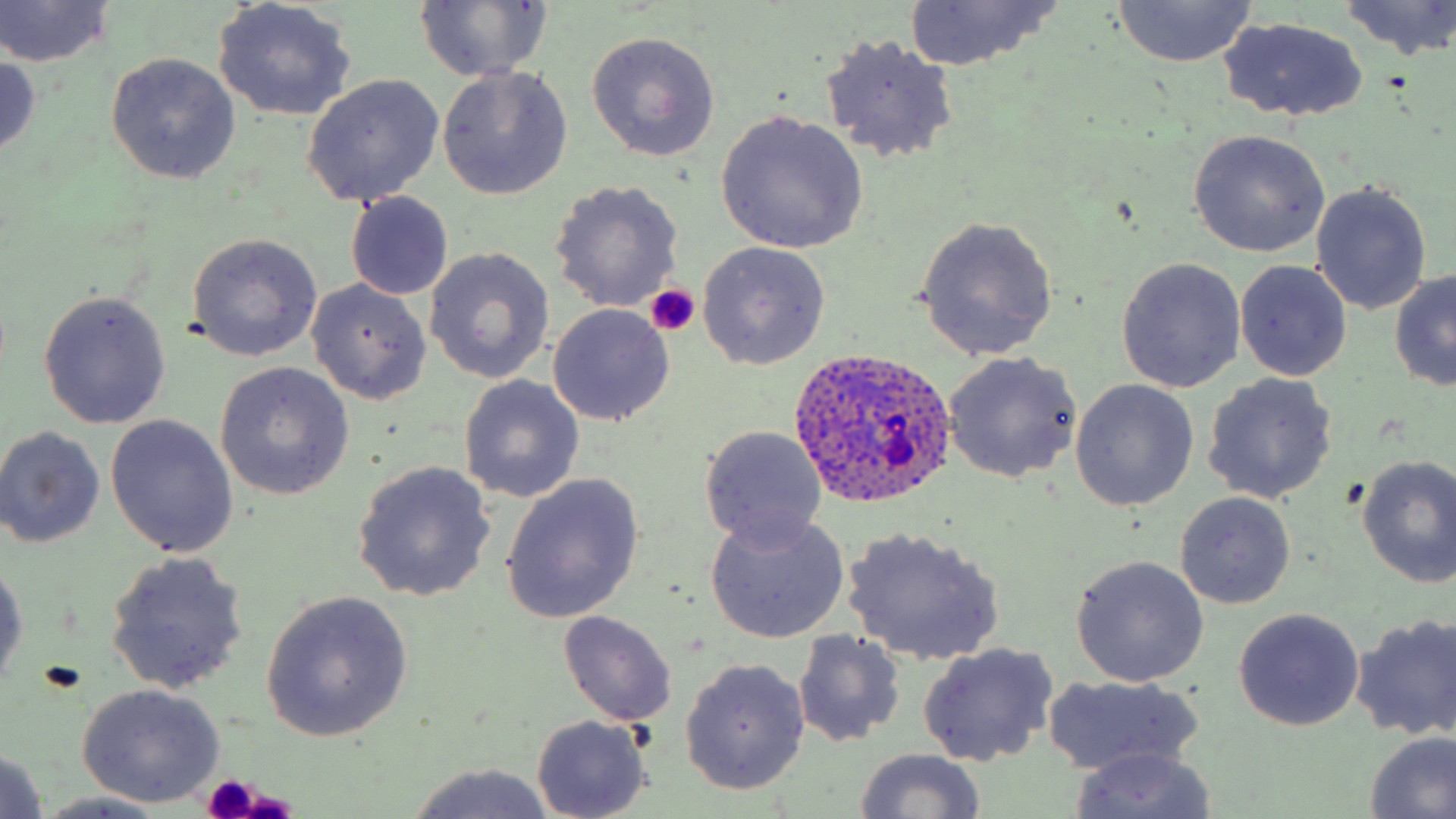

Summary:
  - Coordinate format: approximate bounding boxes as (x1, y1, x2, y2) in pixels
  - Uninfected red blood cell locations: (1339, 0, 1456, 60), (0, 1, 117, 69), (213, 1, 356, 121), (412, 1, 553, 82), (900, 1, 1066, 70), (1111, 1, 1257, 68), (1219, 17, 1369, 123), (586, 30, 721, 162), (819, 33, 959, 163), (0, 52, 44, 161), (104, 52, 242, 184), (437, 66, 572, 199), (302, 75, 443, 207), (713, 110, 871, 255), (1188, 130, 1331, 256), (549, 180, 684, 313), (1311, 184, 1433, 316), (347, 193, 453, 301), (914, 216, 1059, 360), (186, 233, 324, 361), (697, 243, 830, 371), (425, 249, 555, 384), (1116, 257, 1247, 393), (1235, 260, 1353, 381), (1389, 269, 1456, 393), (306, 280, 433, 404), (37, 290, 172, 430), (547, 304, 675, 426), (944, 353, 1081, 485), (214, 363, 354, 500), (1201, 372, 1338, 505), (458, 375, 585, 503), (1068, 380, 1199, 512), (105, 414, 239, 557), (0, 425, 103, 548), (700, 427, 829, 549), (1356, 455, 1456, 586), (352, 461, 497, 601), (499, 473, 645, 621), (1175, 491, 1296, 610), (705, 511, 849, 643), (1126, 511, 1281, 648), (843, 528, 1005, 664), (105, 551, 249, 695), (0, 553, 27, 694), (1071, 556, 1210, 687), (262, 592, 413, 742), (1233, 608, 1365, 731), (557, 610, 676, 727), (1351, 613, 1456, 742), (792, 630, 905, 747), (917, 643, 1060, 767), (679, 658, 810, 795), (1043, 674, 1203, 775), (76, 683, 228, 807), (532, 715, 653, 818), (1364, 732, 1456, 819), (1068, 746, 1220, 818), (0, 747, 48, 819), (853, 750, 985, 817), (402, 763, 556, 819), (33, 793, 178, 818)
  - Plasmodium ovale-infected red blood cell locations: (787, 350, 961, 507)
  - Platelet locations: (643, 284, 702, 338), (202, 773, 264, 818)
  - Slide-level diagnosis: Plasmodium ovale
  - Field of view: one of a larger specimen
  - Image size: 1456×819 pixels
  - Magnification: 1000x
  - Preparation: thin blood smear
  - Modality: optical microscopy
  - Stain: May-Grünwald-Giemsa